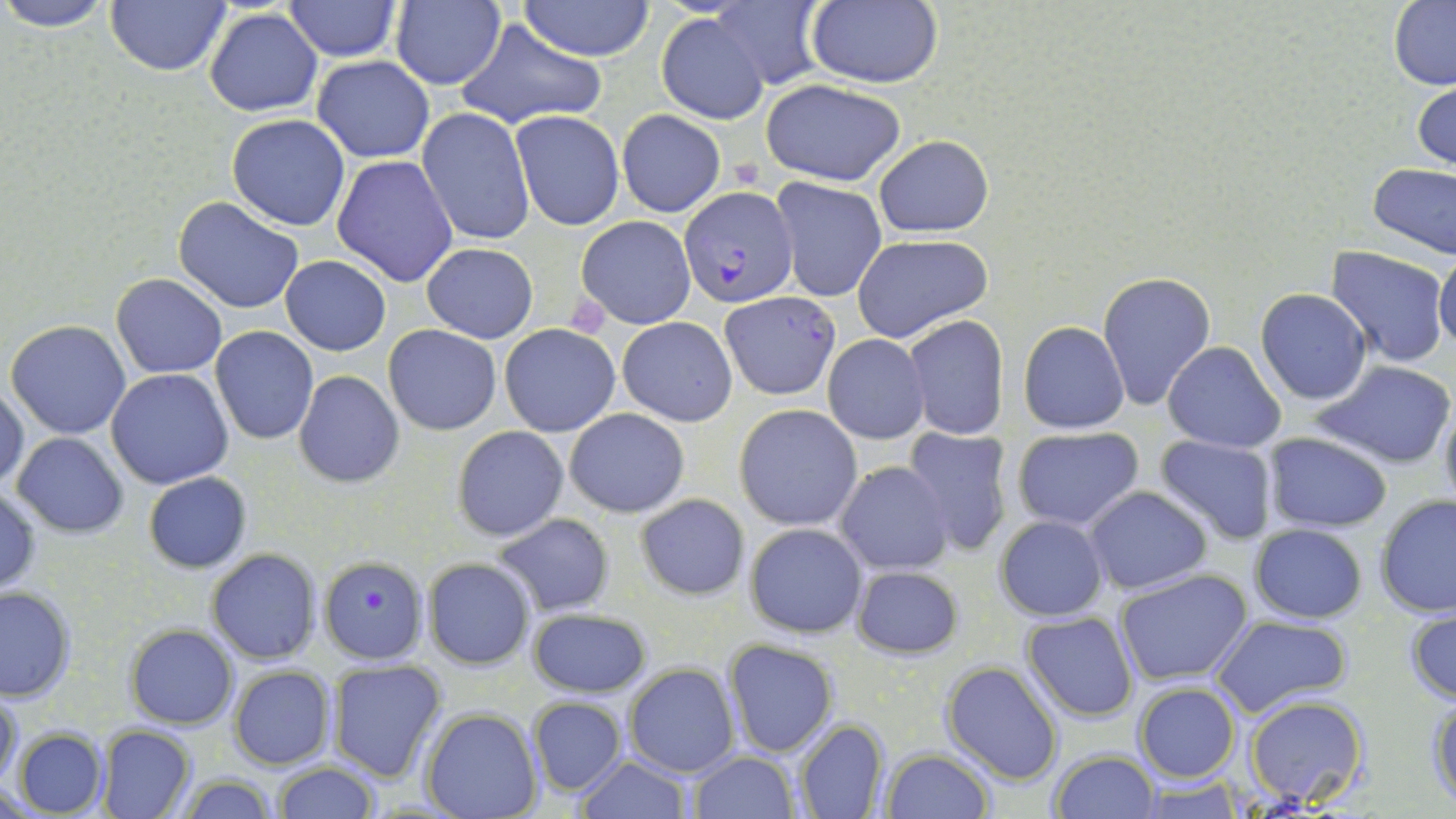 Approximate bounding boxes as (x1, y1, x2, y2) in pixels. Plasmodium falciparum-infected red blood cell locations: (679, 187, 799, 306), (722, 292, 839, 400), (314, 557, 425, 665). Uninfected red blood cell locations: (0, 0, 117, 30), (284, 0, 403, 61), (390, 0, 505, 91), (518, 0, 656, 60), (710, 0, 833, 90), (105, 1, 232, 77), (799, 2, 947, 89), (1388, 2, 1456, 88), (203, 8, 323, 115), (656, 13, 770, 124), (452, 18, 610, 132), (312, 55, 434, 163), (1413, 77, 1456, 173), (760, 78, 908, 186), (416, 106, 536, 246), (510, 109, 625, 231), (616, 109, 725, 216), (227, 113, 351, 231), (873, 135, 994, 238), (331, 155, 460, 288), (1367, 161, 1456, 259), (772, 178, 887, 302), (174, 196, 306, 313), (576, 215, 696, 329), (850, 236, 992, 345), (422, 243, 538, 343), (1327, 247, 1451, 367), (1434, 247, 1456, 357), (279, 256, 390, 355), (1096, 271, 1217, 411), (111, 273, 228, 380), (1256, 288, 1371, 405), (903, 315, 1008, 438), (616, 317, 738, 426), (6, 318, 132, 438), (1019, 321, 1130, 433), (499, 322, 621, 437), (383, 324, 502, 435), (210, 326, 318, 445), (822, 333, 930, 444), (1164, 341, 1287, 453), (1312, 360, 1455, 470), (105, 368, 234, 490), (293, 370, 405, 489), (1, 380, 28, 492), (1437, 392, 1456, 523), (734, 404, 863, 531), (564, 409, 690, 516), (453, 427, 569, 541), (901, 427, 1012, 557), (1010, 428, 1146, 532), (1263, 431, 1393, 532), (12, 433, 129, 536), (1154, 435, 1277, 545), (835, 461, 955, 574), (144, 472, 251, 573), (1085, 485, 1212, 594), (0, 486, 42, 597), (634, 494, 750, 600), (1375, 495, 1456, 620), (492, 512, 615, 618), (994, 514, 1109, 622), (744, 522, 867, 638), (1249, 522, 1368, 624), (205, 549, 322, 663), (423, 558, 535, 669), (851, 563, 964, 660), (1114, 568, 1253, 686), (0, 587, 76, 702), (1406, 602, 1455, 705), (526, 607, 652, 699), (1022, 611, 1139, 722), (1208, 615, 1355, 718), (125, 625, 237, 729), (722, 638, 839, 756), (327, 660, 446, 781), (942, 660, 1064, 785), (623, 662, 738, 778), (227, 665, 336, 769), (1133, 682, 1240, 782), (1, 689, 22, 789), (1427, 691, 1456, 808), (1244, 695, 1369, 809), (527, 696, 629, 796), (421, 709, 542, 819), (794, 718, 890, 819), (96, 723, 196, 819), (13, 728, 107, 818), (881, 748, 993, 819), (1049, 749, 1158, 818), (689, 752, 798, 819), (574, 755, 692, 819), (274, 762, 379, 819), (177, 776, 279, 816), (1135, 779, 1244, 815). Platelet locations: (566, 295, 610, 338). Slide-level diagnosis: Plasmodium falciparum. Captured at 1000x magnification. Image is 1456×819 pixels. Thin blood smear. One field of a larger specimen. Light microscopy. May-Grünwald-Giemsa stain.